State the preparation type.
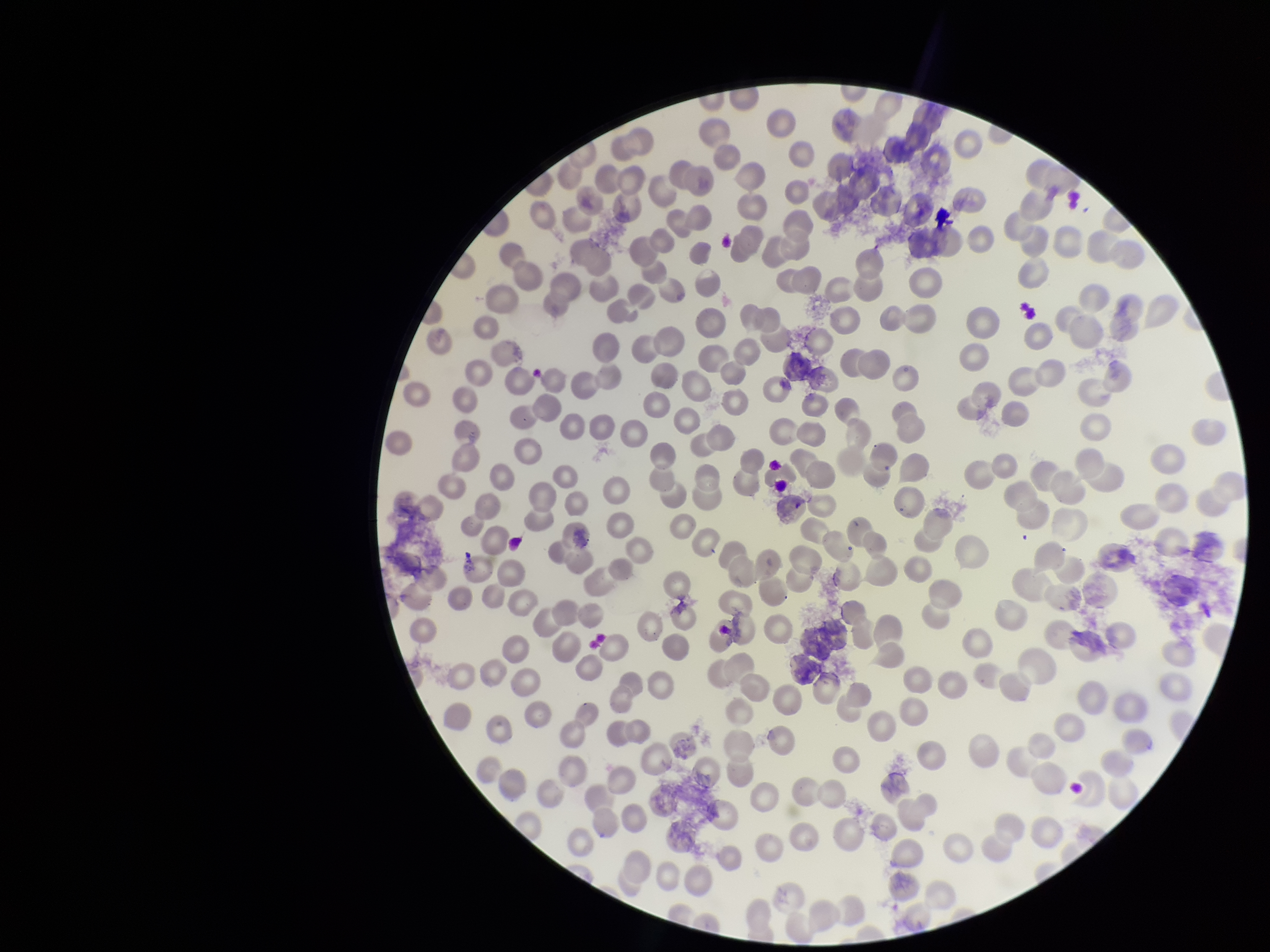

It is a thin blood smear.

red blood cell count = 252
image size = 1270×952 pixels
parasitized red blood cell count = 0
parasitized red blood cells = none seen
field of view = single
stain = Giemsa
patient malaria status = negative
capture = smartphone photograph through the microscope eyepiece